Assess this cell for malaria.
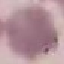
Uninfected.

Photographed with a smartphone camera at the microscope eyepiece. Thin smear of blood. Giemsa-stained preparation. Automatically extracted cell patch, resized to 64 × 64 pixels.